Outline each Plasmodium ovale-infected red blood cell.
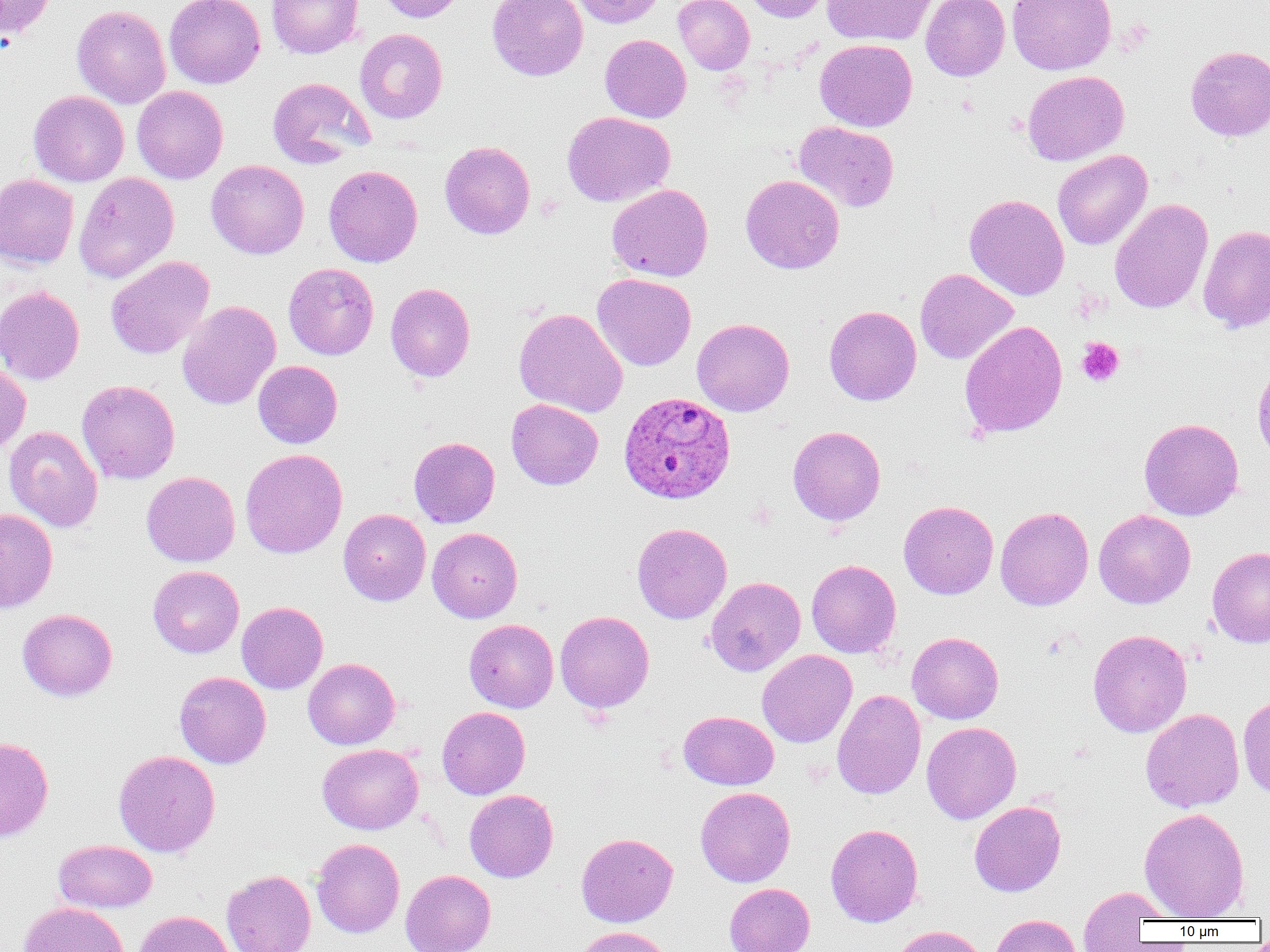
Approximate bounding boxes as [x1, y1, x2, y2] in pixels.
Plasmodium ovale-infected red blood cells: [618, 391, 735, 504].

Summary:
  - Uninfected red blood cell locations: [0, 0, 57, 42], [164, 0, 265, 89], [267, 0, 363, 59], [375, 0, 466, 23], [487, 0, 588, 80], [571, 0, 666, 28], [673, 0, 754, 74], [742, 0, 832, 23], [821, 0, 937, 46], [920, 0, 1010, 81], [1007, 0, 1116, 75], [72, 5, 171, 109], [354, 28, 448, 124], [600, 34, 691, 122], [815, 39, 917, 132], [1185, 45, 1270, 141], [1022, 70, 1129, 165], [267, 77, 373, 169], [132, 86, 229, 184], [28, 90, 129, 187], [562, 111, 675, 206], [793, 120, 899, 212], [440, 141, 535, 239], [1053, 149, 1153, 250], [206, 160, 309, 259], [323, 164, 423, 267], [73, 172, 179, 284], [0, 174, 79, 270], [740, 174, 844, 274], [606, 183, 713, 282], [964, 193, 1069, 300], [1109, 199, 1213, 314], [1198, 224, 1270, 334], [106, 256, 214, 359], [283, 263, 379, 360], [915, 268, 1018, 365], [592, 273, 696, 371], [385, 283, 475, 381], [0, 285, 85, 384], [177, 300, 281, 410], [824, 305, 921, 405], [514, 308, 628, 417], [692, 318, 794, 416], [959, 321, 1068, 438], [253, 360, 342, 448], [0, 362, 31, 457], [76, 380, 180, 484], [506, 399, 603, 490], [1139, 418, 1244, 521], [4, 425, 103, 532], [787, 425, 885, 526], [409, 437, 499, 528], [240, 448, 347, 559], [141, 471, 240, 567], [898, 500, 998, 599], [995, 506, 1094, 611], [0, 508, 58, 613], [338, 508, 431, 606], [1093, 509, 1196, 609], [631, 522, 732, 624], [427, 527, 522, 623], [1207, 546, 1270, 648], [806, 559, 901, 658], [148, 565, 244, 658], [706, 576, 805, 676], [236, 601, 328, 694], [17, 608, 117, 701], [555, 610, 654, 713], [464, 619, 558, 712], [1088, 629, 1192, 737], [907, 631, 1004, 724], [757, 649, 857, 748], [303, 657, 400, 750], [174, 671, 271, 769], [832, 689, 926, 799], [1237, 694, 1270, 799], [437, 707, 530, 799], [1141, 708, 1244, 813], [679, 711, 779, 790], [921, 721, 1021, 824], [0, 736, 54, 843], [317, 744, 423, 834], [113, 749, 220, 857], [695, 786, 795, 887], [464, 789, 558, 882], [969, 801, 1066, 897], [1139, 807, 1250, 920], [825, 823, 924, 927], [576, 833, 678, 927], [311, 838, 405, 938], [53, 840, 157, 913], [222, 869, 315, 952], [400, 869, 496, 952], [725, 882, 815, 952], [1077, 886, 1168, 950], [18, 901, 129, 952], [134, 910, 237, 952], [989, 914, 1081, 952], [890, 925, 989, 952], [576, 926, 673, 952]
  - Platelet locations: [1077, 337, 1124, 387]
  - Slide-level diagnosis: Plasmodium ovale
  - Field of view: one of a larger specimen
  - Preparation: thin blood smear
  - Image size: 1270×952 pixels
  - Magnification: 1000x
  - Modality: optical microscopy